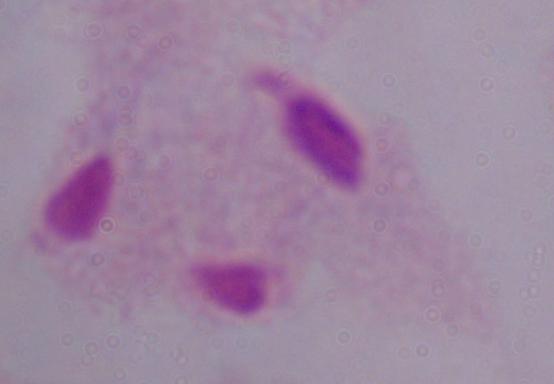
Captured at 1000x magnification. Photomicrograph. A trichomonad is seen.